Describe the morphology of the erythrocytes.
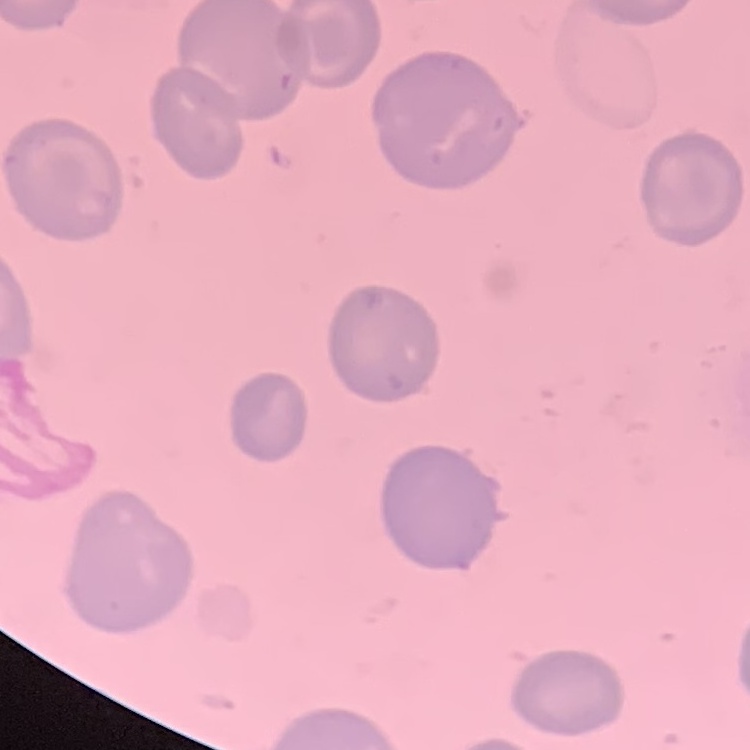

No rouleaux formation.

Summary:
  - Image type: square crop of a larger photomicrograph
  - Preparation: thin peripheral smear
  - Stain: Field's or Giemsa